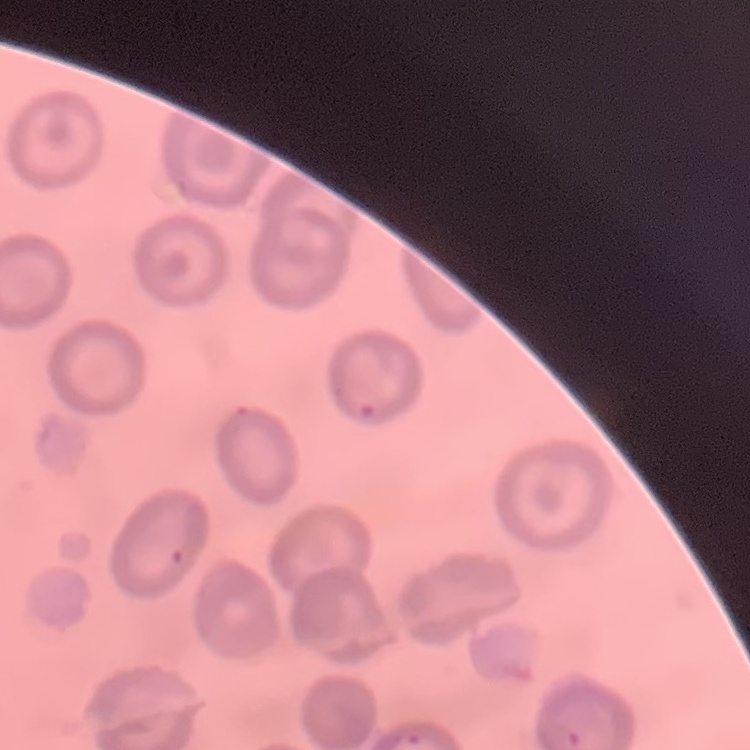

erythrocyte morphology = no rouleaux formation
stain = Field's or Giemsa
image type = square crop of a larger photomicrograph
preparation = thin blood film